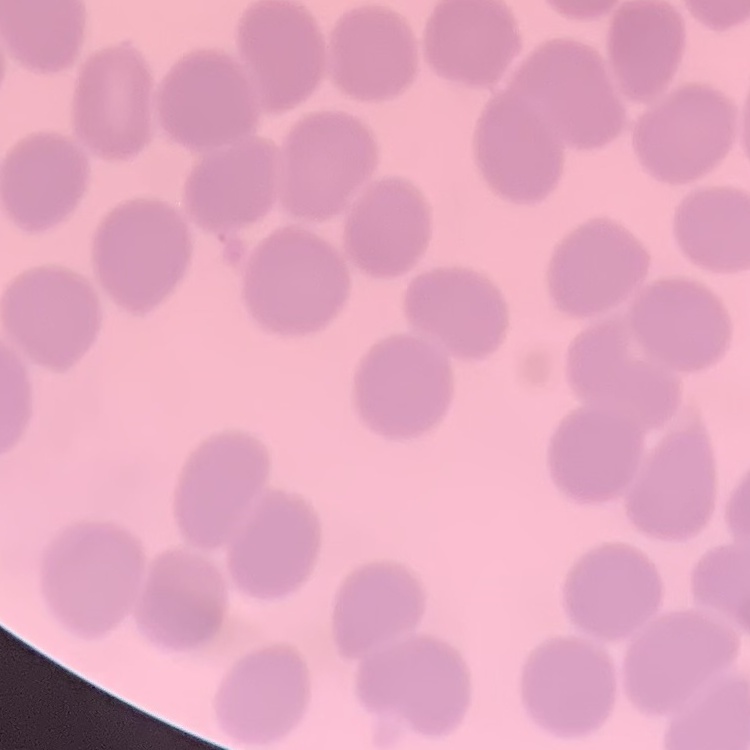

red_blood_cell_morphology: no rouleaux formation
stain: Field's or Giemsa
preparation: thin peripheral smear
image_type: one tile cut from a larger photomicrograph